Comment on the morphology of the red blood cells.
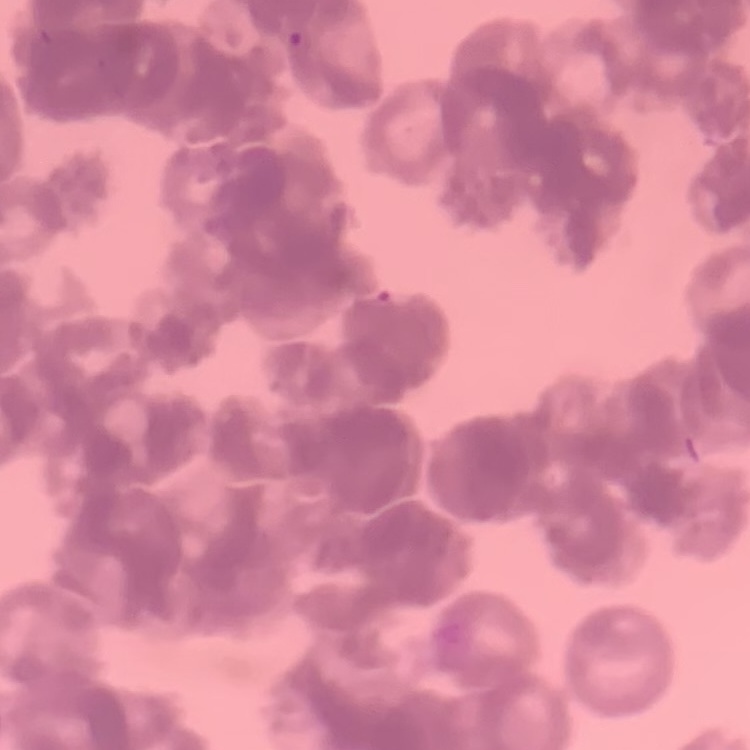

They show rouleaux formation.

preparation: thin blood smear
image_type: square crop of a larger photomicrograph
stain: Field's or Giemsa